Name the parasite shown.
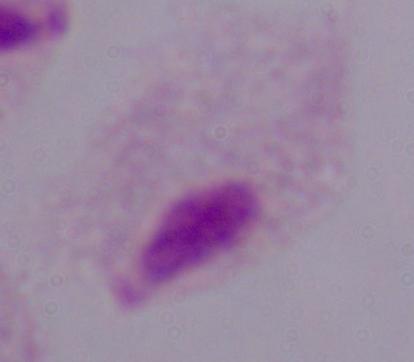
A trichomonad.

Captured at 1000x magnification. Photomicrograph.